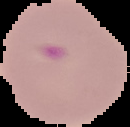
image size = 130×127 pixels
malaria status = parasitized
preparation = thin blood film
image type = segmented cell region with the area outside set to black